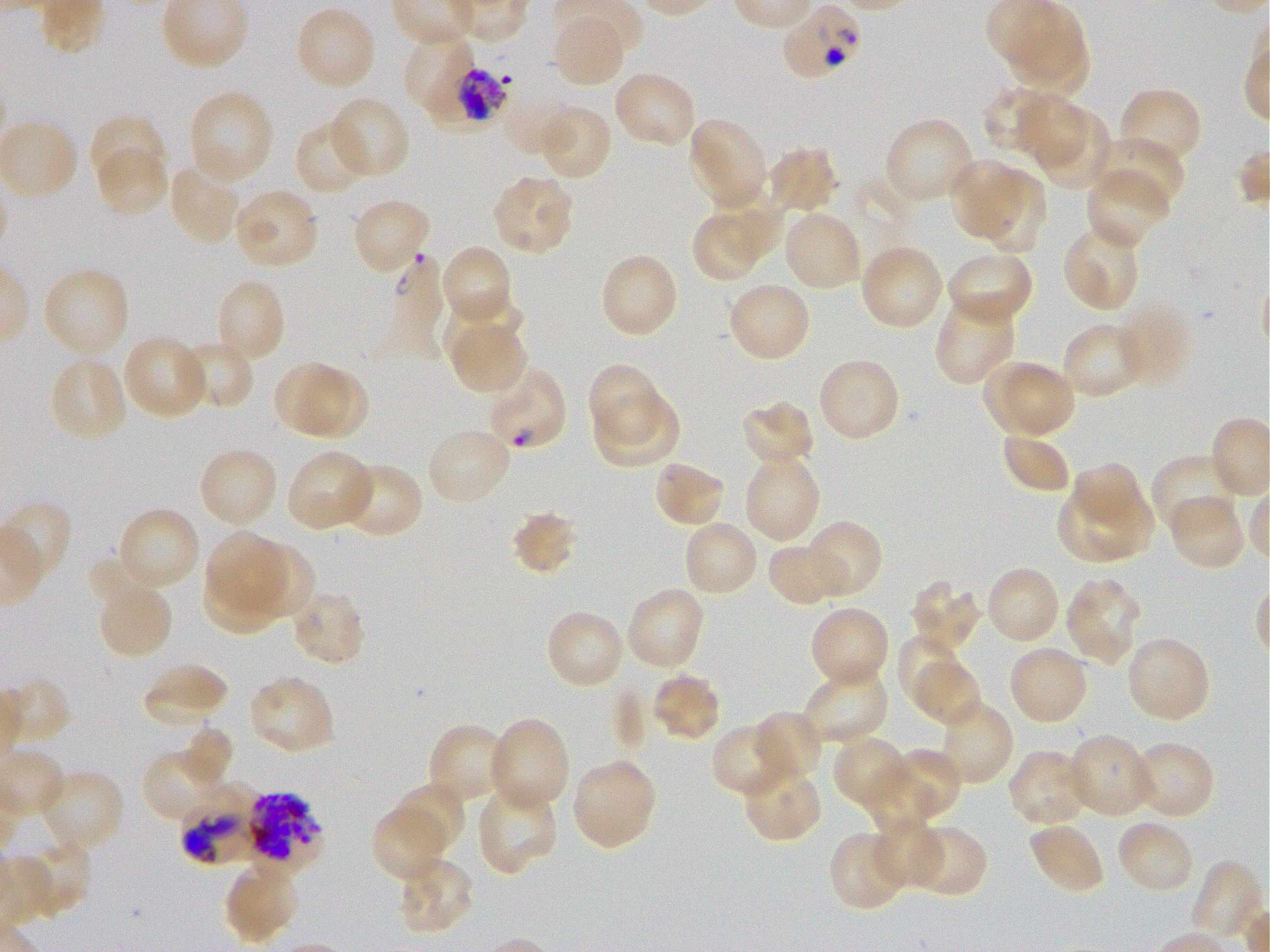

Approximate bounding boxes as (x1, y1, x2, y2) in pixels. Not every red blood cell is marked. A life-cycle stage — or a range of stages, where the recorded stages span more than one — follows each staged infected red blood cell. Locations of red blood cells of indeterminate infection status: (782, 3, 868, 79), (178, 785, 268, 867), (244, 792, 323, 869). Locations of infected red blood cells: (428, 54, 516, 140) early trophozoite to early schizont; (386, 255, 448, 339) ring; (485, 364, 568, 451) ring. Locations of uninfected red blood cells: (293, 5, 377, 92), (1016, 5, 1085, 73), (552, 12, 629, 88), (1012, 29, 1089, 99), (402, 30, 479, 120), (611, 69, 697, 149), (1118, 87, 1202, 171), (980, 88, 1054, 153), (186, 89, 273, 186), (327, 95, 411, 181), (1020, 99, 1088, 169), (1024, 101, 1110, 192), (537, 104, 613, 183), (89, 109, 173, 178), (687, 116, 770, 212), (882, 116, 975, 205), (294, 120, 370, 196), (1094, 136, 1185, 214), (95, 142, 170, 218), (764, 146, 838, 214), (949, 159, 1026, 237), (168, 160, 244, 245), (1085, 168, 1172, 250), (983, 172, 1047, 254), (490, 173, 575, 257), (711, 182, 784, 258), (231, 188, 320, 271), (351, 197, 432, 277), (782, 209, 863, 292), (693, 217, 758, 282), (1061, 223, 1142, 312), (439, 243, 511, 323), (858, 243, 944, 331), (944, 249, 1034, 328), (598, 252, 679, 339), (40, 266, 131, 361), (213, 278, 287, 366), (726, 281, 811, 363), (934, 296, 1017, 386), (442, 300, 525, 356), (1117, 303, 1192, 389), (1060, 321, 1147, 400), (452, 328, 526, 391), (122, 334, 210, 420), (177, 339, 255, 410), (49, 355, 128, 444), (816, 356, 901, 443), (983, 358, 1076, 439), (272, 360, 355, 435), (586, 363, 662, 445), (299, 368, 372, 452), (596, 393, 680, 466), (741, 399, 816, 467), (426, 425, 514, 506), (1001, 429, 1072, 494), (197, 446, 279, 529), (285, 450, 376, 532), (742, 451, 820, 544), (1152, 454, 1241, 538), (652, 459, 727, 528), (1070, 460, 1148, 523), (333, 462, 422, 539), (1057, 475, 1156, 564), (1167, 494, 1248, 571), (0, 499, 77, 603), (115, 506, 202, 593), (512, 511, 577, 574), (682, 519, 760, 598), (802, 520, 881, 599), (203, 532, 292, 615), (246, 538, 317, 619), (767, 539, 851, 607), (984, 565, 1061, 645), (200, 569, 292, 640), (1063, 577, 1142, 666), (909, 580, 981, 654), (100, 582, 172, 661), (624, 585, 707, 673), (289, 587, 366, 666), (808, 605, 891, 690), (545, 609, 626, 690), (895, 634, 958, 706), (1125, 635, 1212, 724), (1007, 644, 1089, 727), (141, 660, 230, 727), (915, 661, 983, 727), (800, 667, 889, 746), (651, 672, 721, 741), (246, 674, 337, 756), (941, 705, 1014, 786), (752, 710, 824, 786), (488, 717, 570, 814), (710, 722, 794, 798), (427, 723, 512, 806), (177, 724, 234, 790), (1066, 732, 1156, 819), (832, 735, 908, 806), (1127, 740, 1216, 820), (142, 747, 230, 826), (891, 748, 958, 818), (1007, 749, 1092, 828), (570, 757, 658, 852), (740, 761, 823, 842), (36, 769, 125, 853), (868, 771, 935, 839), (389, 783, 466, 856), (476, 784, 558, 875), (371, 804, 450, 881), (1114, 817, 1196, 896), (875, 825, 944, 885), (912, 826, 988, 897), (1031, 827, 1103, 889), (828, 831, 902, 906), (12, 834, 93, 919), (395, 855, 475, 936), (1189, 859, 1265, 943), (223, 860, 300, 946). 100x objective under oil immersion, numerical aperture 1.25. Giemsa stain. Image is 1270×952 pixels. Donor blood group O+. Plasmodium falciparum strain 3D7 in static in-vitro culture. One field from this slide. Thin blood smear.